Report the malaria status of this cell.
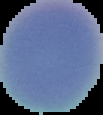
It is uninfected.

{
  "image_type": "segmented cell region with the area outside set to black",
  "image_size": "103×115 pixels",
  "preparation": "thin blood film"
}